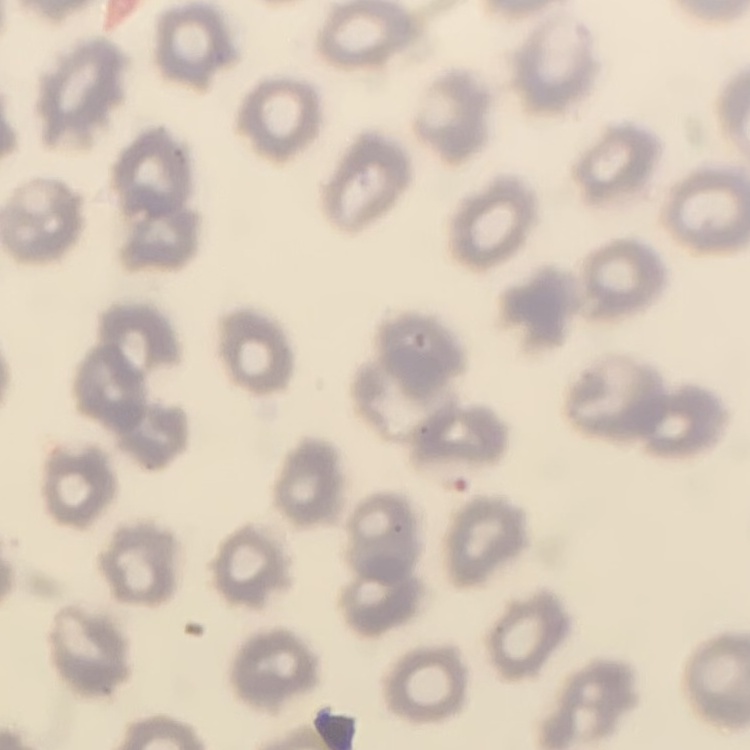

The red blood cells show no rouleaux formation. Stained with either Field's or Giemsa. Thin blood smear. One tile cut from a larger photomicrograph.